State which parasite is depicted.
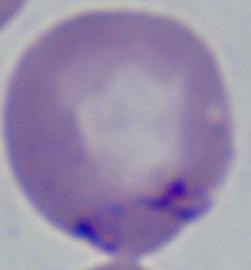
Babesia.

modality = photomicrograph
magnification = 1000x